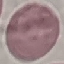

Summary:
  - Result: no malaria parasites detected
  - Preparation: thin blood film
  - Stain: Giemsa
  - Image type: automatically extracted cell patch, resized to 64 × 64 pixels
  - Capture: smartphone camera at the microscope eyepiece